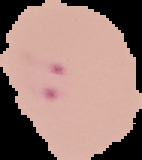
preparation = thin blood smear
result = malaria parasites detected
image type = segmented cell region on a black background
image size = 142×160 pixels